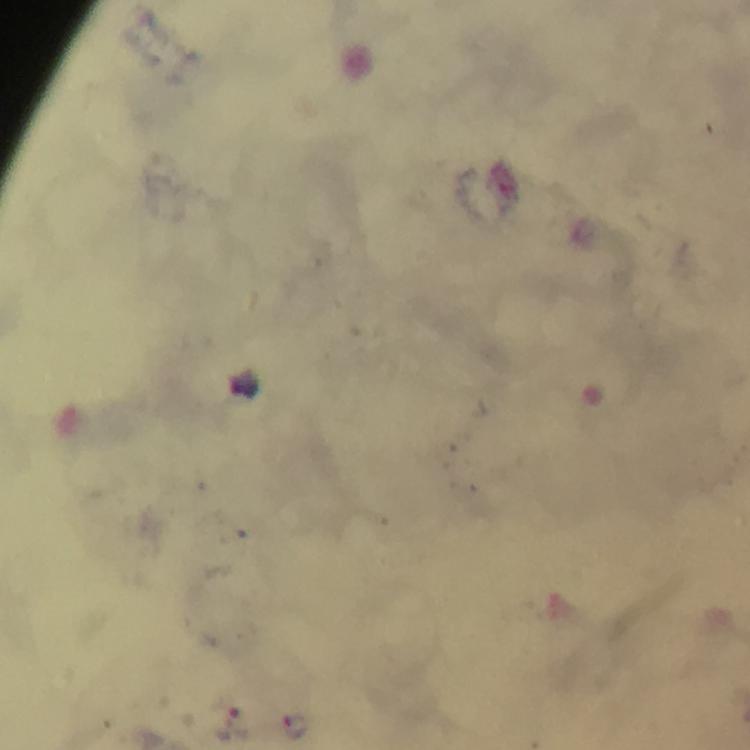

{
  "image_size": "750×750 pixels",
  "stain": "Giemsa",
  "magnification": "100x",
  "capture": "smartphone photograph through a microscope",
  "cropped_from": "a single field of view",
  "immersion_oil": "used",
  "context": "from a malaria diagnostic workup",
  "plasmodium_parasite_locations": "approximate object centers, in pixels from the top-left corner: (x=239, y=725), (x=297, y=725)",
  "preparation": "thick blood smear"
}